Identify the cell.
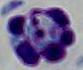

A leukocyte.

modality: micrograph
magnification: 1000x